Name the cell type shown.
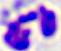
This is a leukocyte.

400x magnification. Photomicrograph.